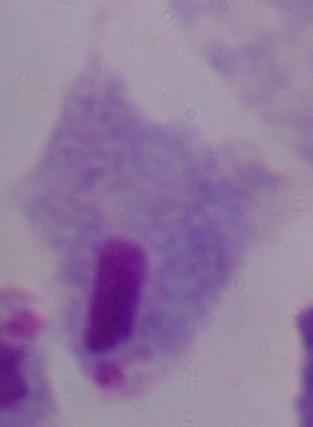

modality = photomicrograph
identification = trichomonad
magnification = 1000x